Report the malaria status of this cell.
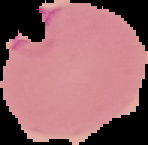

Parasitized.

Summary:
  - Image type: segmented cell region with the area outside set to black
  - Preparation: thin blood film
  - Image size: 148×145 pixels